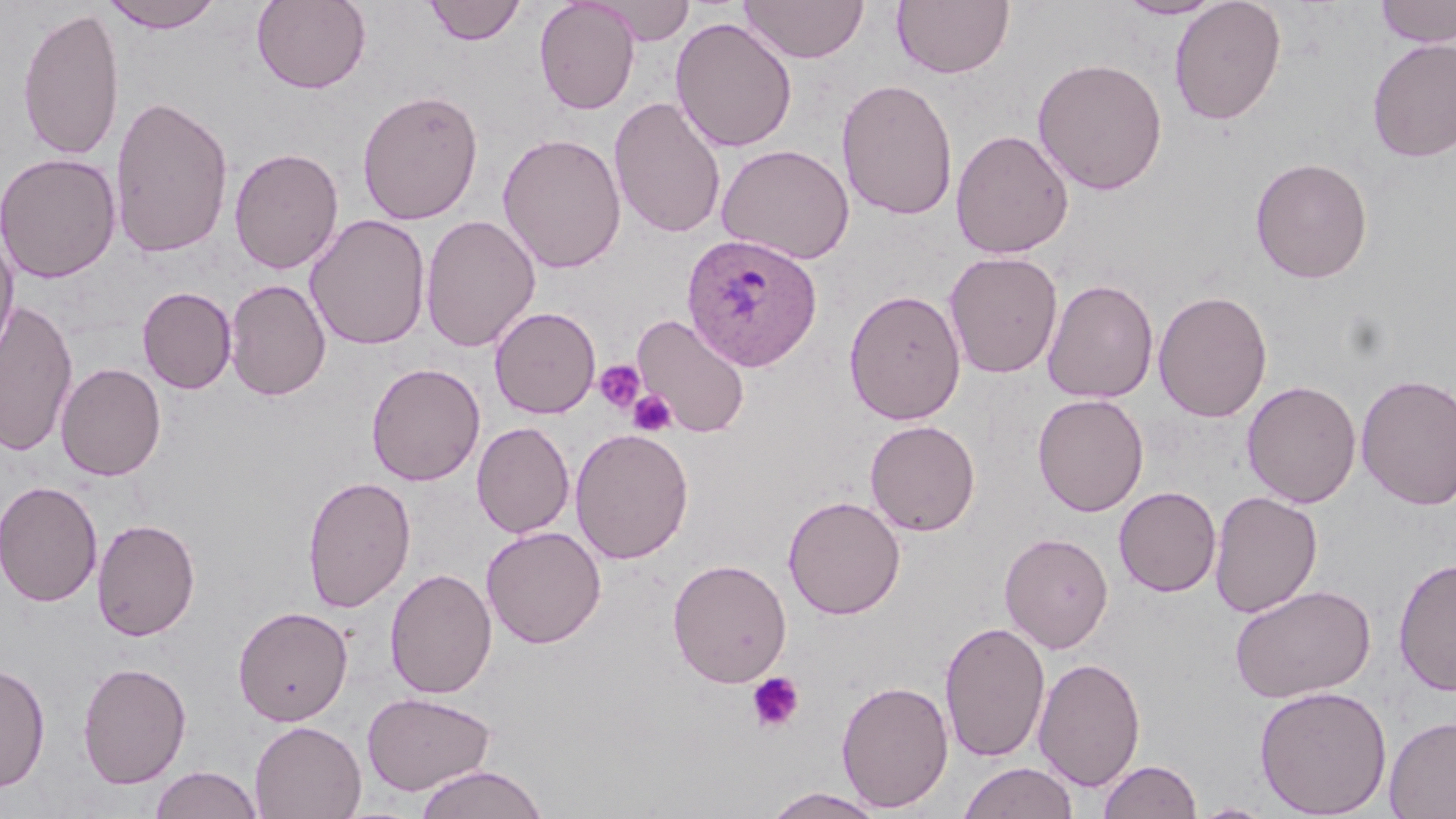
slide-level diagnosis = Plasmodium ovale
stain = May-Grünwald-Giemsa
modality = light microscopy
uninfected red blood cell locations = approximate bounding boxes as (x1,y1)-(x2,y2) corner pairs in pixels: (101,0)-(225,33), (251,0)-(371,94), (424,0)-(526,45), (534,0)-(640,115), (739,0)-(869,63), (1116,0)-(1225,20), (1169,0)-(1287,126), (1375,0)-(1456,47), (594,1)-(695,45), (892,1)-(1015,79), (16,5)-(125,163), (670,16)-(798,153), (1366,38)-(1456,162), (1032,57)-(1168,195), (836,78)-(958,221), (356,89)-(484,226), (109,93)-(234,260), (608,96)-(727,240), (951,129)-(1074,258), (497,132)-(626,274), (716,143)-(855,264), (229,147)-(344,275), (0,152)-(122,283), (1250,157)-(1374,284), (305,214)-(431,350), (420,214)-(540,353), (0,229)-(19,369), (944,251)-(1063,378), (224,278)-(331,401), (1042,278)-(1158,403), (137,286)-(237,394), (843,289)-(966,425), (1153,290)-(1272,422), (1,299)-(78,457), (489,307)-(601,419), (632,312)-(751,438), (56,362)-(165,481), (366,363)-(485,486), (1356,373)-(1456,510), (1242,380)-(1361,508), (1032,394)-(1149,516), (864,420)-(980,537), (471,421)-(574,538), (570,427)-(694,565), (302,474)-(416,613), (0,480)-(103,607), (1114,486)-(1221,597), (1209,490)-(1323,618), (783,495)-(906,619), (92,518)-(201,641), (481,526)-(606,648), (999,532)-(1113,653), (1393,556)-(1456,696), (667,558)-(792,687), (385,568)-(498,700), (1229,584)-(1376,703), (233,605)-(353,725), (939,620)-(1051,763), (1033,656)-(1146,791), (0,661)-(51,792), (77,661)-(191,788), (836,679)-(954,812), (1254,685)-(1392,818), (361,691)-(497,796), (1384,715)-(1456,818), (249,720)-(366,819), (1098,758)-(1202,819), (958,761)-(1079,819), (149,765)-(264,819), (413,765)-(549,819), (760,787)-(888,819), (1192,802)-(1276,818)
platelet locations = approximate bounding boxes as (x1,y1)-(x2,y2) corner pairs in pixels: (593,360)-(646,414), (628,389)-(677,436), (746,671)-(805,733)
field of view = single
preparation = thin blood film
image size = 1456×819 pixels
magnification = 1000x
Plasmodium ovale-infected red blood cell locations = approximate bounding boxes as (x1,y1)-(x2,y2) corner pairs in pixels: (681,233)-(823,372)